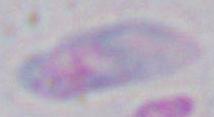

{
  "magnification": "1000x",
  "identification": "Toxoplasma gondii",
  "modality": "micrograph"
}